State the preparation type.
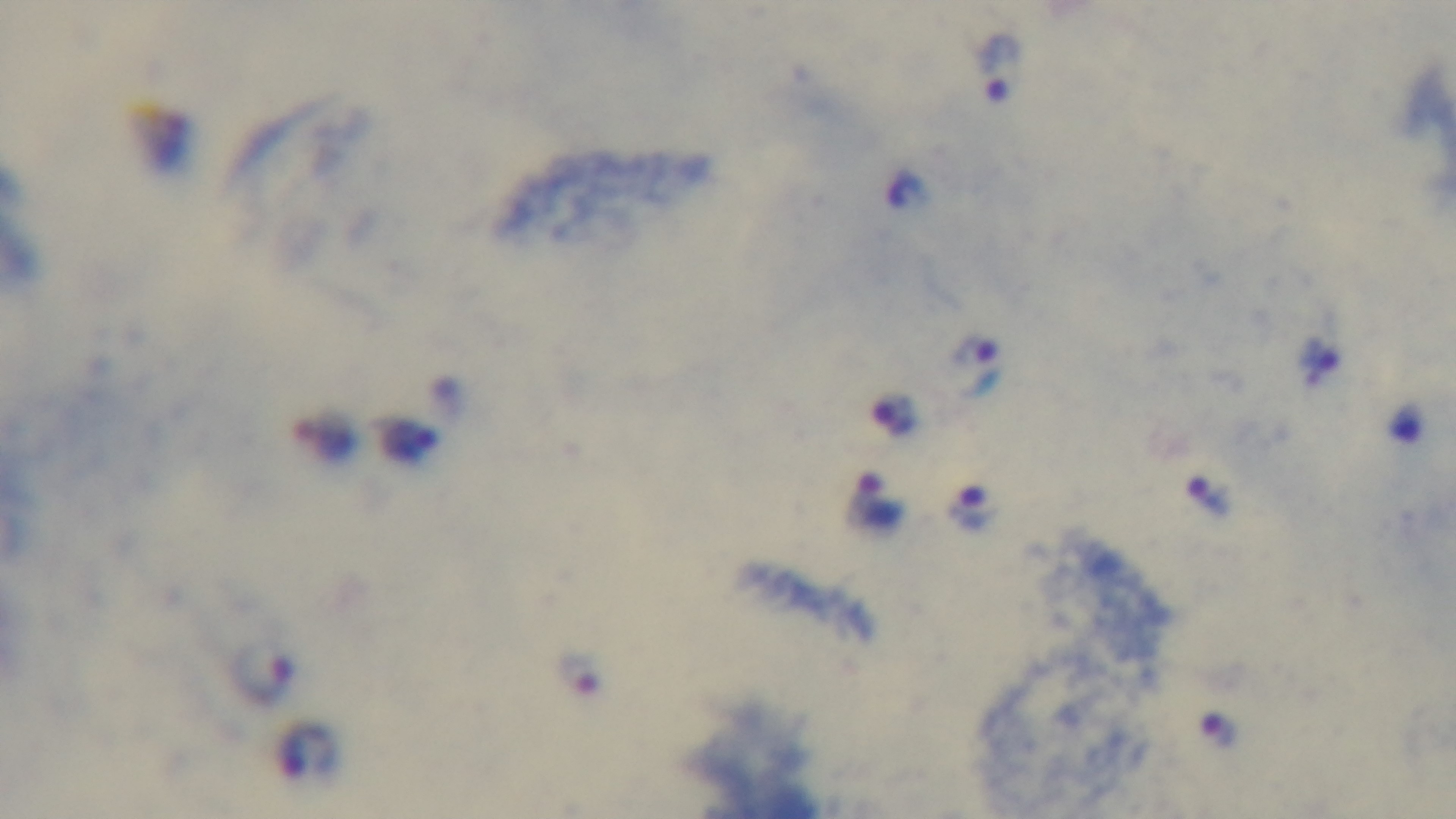

Thick.

Light microscopy. Mounted 4K digital camera. Oil-immersion objective, 100x. Giemsa-stained. Single field of view. Malaria status: infected.